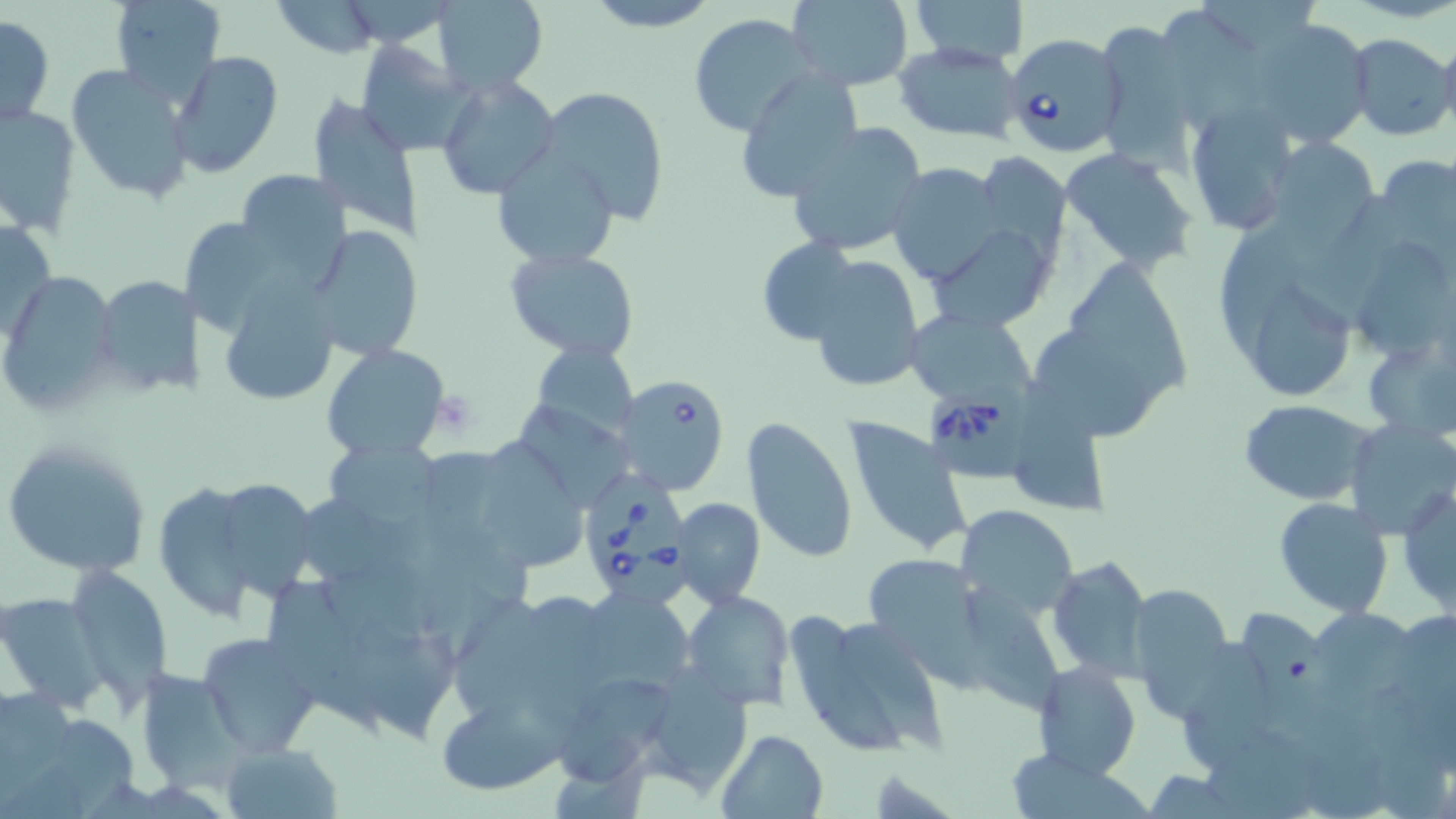
Summary:
  - Coordinate format: approximate bounding boxes as named x1/y1/x2/y2 corners in pixels
  - Babesia divergens-infected red blood cell locations: (x1=1003, y1=31, x2=1126, y2=158), (x1=613, y1=375, x2=733, y2=497), (x1=929, y1=378, x2=1044, y2=478), (x1=581, y1=463, x2=694, y2=608)
  - Uninfected red blood cell locations: (x1=107, y1=0, x2=227, y2=102), (x1=432, y1=0, x2=550, y2=95), (x1=579, y1=0, x2=722, y2=31), (x1=786, y1=0, x2=914, y2=89), (x1=909, y1=0, x2=1030, y2=67), (x1=270, y1=1, x2=385, y2=58), (x1=688, y1=13, x2=813, y2=133), (x1=0, y1=14, x2=54, y2=128), (x1=1241, y1=16, x2=1373, y2=146), (x1=1106, y1=23, x2=1197, y2=172), (x1=1437, y1=31, x2=1456, y2=139), (x1=1345, y1=34, x2=1456, y2=141), (x1=354, y1=38, x2=473, y2=156), (x1=893, y1=42, x2=1024, y2=145), (x1=167, y1=50, x2=285, y2=178), (x1=67, y1=63, x2=195, y2=203), (x1=731, y1=70, x2=862, y2=201), (x1=436, y1=75, x2=562, y2=202), (x1=536, y1=85, x2=669, y2=225), (x1=306, y1=97, x2=423, y2=237), (x1=1185, y1=101, x2=1299, y2=235), (x1=1, y1=102, x2=81, y2=237), (x1=786, y1=123, x2=927, y2=259), (x1=1263, y1=137, x2=1381, y2=244), (x1=491, y1=147, x2=621, y2=269), (x1=1058, y1=147, x2=1201, y2=273), (x1=978, y1=152, x2=1069, y2=260), (x1=1390, y1=155, x2=1456, y2=258), (x1=886, y1=162, x2=1007, y2=285), (x1=229, y1=170, x2=349, y2=281), (x1=1298, y1=193, x2=1414, y2=331), (x1=1, y1=212, x2=55, y2=347), (x1=928, y1=222, x2=1056, y2=333), (x1=305, y1=225, x2=426, y2=362), (x1=1221, y1=232, x2=1310, y2=354), (x1=754, y1=236, x2=863, y2=342), (x1=1357, y1=245, x2=1448, y2=360), (x1=504, y1=247, x2=640, y2=361), (x1=805, y1=256, x2=924, y2=391), (x1=1074, y1=266, x2=1196, y2=392), (x1=2, y1=273, x2=116, y2=413), (x1=94, y1=273, x2=199, y2=396), (x1=218, y1=273, x2=345, y2=412), (x1=1257, y1=285, x2=1360, y2=400), (x1=910, y1=311, x2=1038, y2=401), (x1=1041, y1=338, x2=1159, y2=446), (x1=1364, y1=341, x2=1452, y2=440), (x1=534, y1=342, x2=637, y2=438), (x1=323, y1=344, x2=451, y2=461), (x1=1017, y1=396, x2=1114, y2=517), (x1=1240, y1=399, x2=1377, y2=505), (x1=519, y1=409, x2=640, y2=515), (x1=1347, y1=417, x2=1456, y2=539), (x1=741, y1=419, x2=857, y2=562), (x1=843, y1=420, x2=971, y2=559), (x1=322, y1=437, x2=447, y2=532), (x1=484, y1=438, x2=591, y2=571), (x1=2, y1=439, x2=156, y2=578), (x1=161, y1=477, x2=257, y2=624), (x1=1396, y1=482, x2=1456, y2=618), (x1=220, y1=484, x2=317, y2=601), (x1=671, y1=497, x2=766, y2=608), (x1=1274, y1=497, x2=1394, y2=616), (x1=955, y1=505, x2=1078, y2=620), (x1=860, y1=553, x2=989, y2=682), (x1=1048, y1=553, x2=1152, y2=680), (x1=66, y1=564, x2=173, y2=704), (x1=1125, y1=583, x2=1236, y2=718), (x1=964, y1=584, x2=1065, y2=712), (x1=270, y1=585, x2=384, y2=734), (x1=589, y1=590, x2=701, y2=694), (x1=682, y1=591, x2=794, y2=710), (x1=2, y1=593, x2=106, y2=712), (x1=1322, y1=602, x2=1424, y2=701), (x1=786, y1=609, x2=947, y2=762), (x1=352, y1=622, x2=463, y2=745), (x1=1184, y1=630, x2=1280, y2=777), (x1=197, y1=632, x2=322, y2=757), (x1=1031, y1=662, x2=1142, y2=780), (x1=635, y1=664, x2=753, y2=793), (x1=135, y1=667, x2=249, y2=789), (x1=557, y1=674, x2=679, y2=782), (x1=434, y1=690, x2=563, y2=796), (x1=715, y1=729, x2=830, y2=818), (x1=220, y1=741, x2=342, y2=818)
  - Platelet locations: (x1=432, y1=392, x2=479, y2=437)
  - Slide-level diagnosis: Babesia divergens
  - Field of view: single
  - Stain: May-Grünwald-Giemsa
  - Modality: optical microscopy
  - Magnification: 1000x
  - Preparation: thin blood smear
  - Image size: 1456×819 pixels